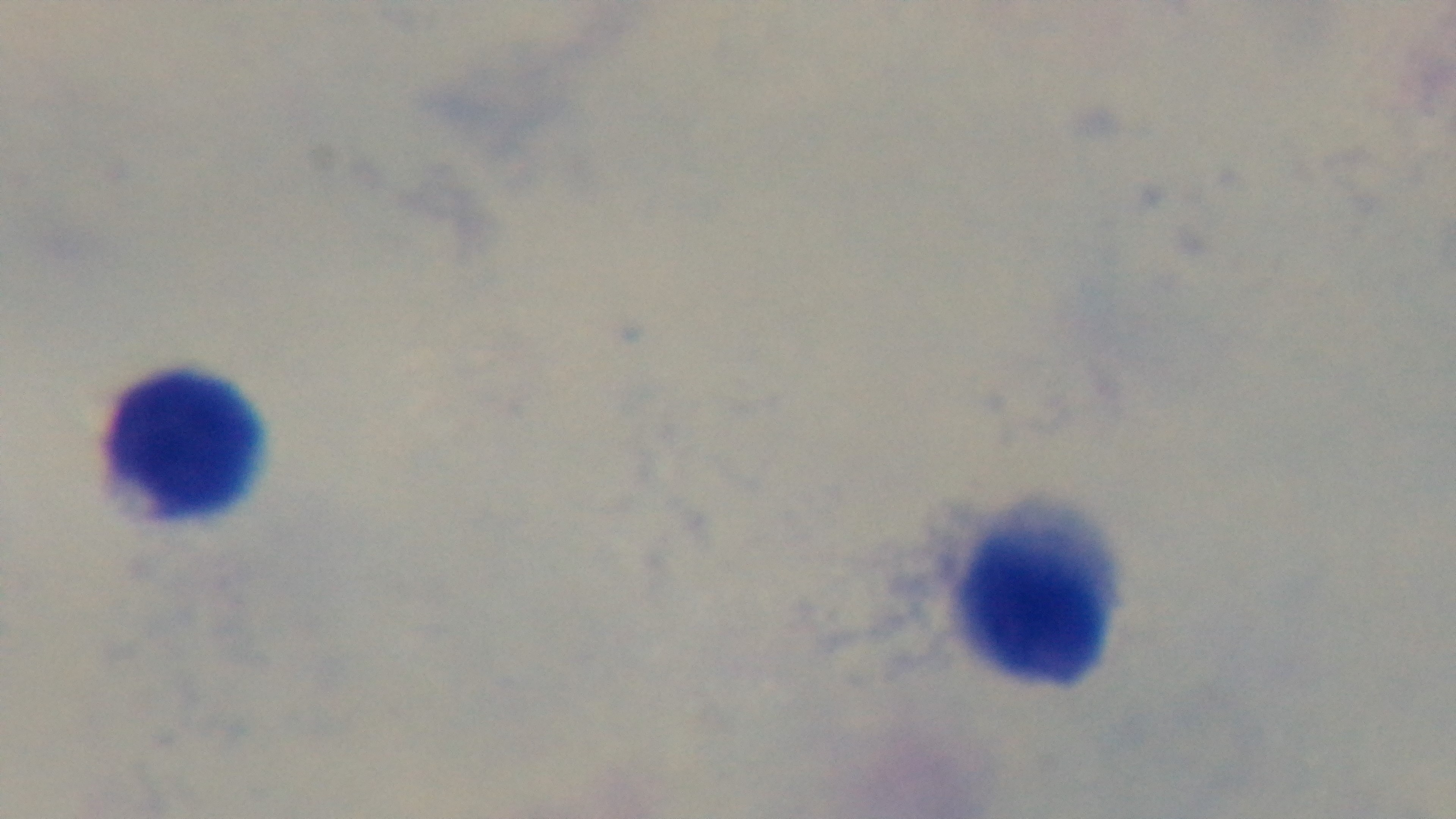
modality = light microscopy
malaria status = uninfected
capture = mounted 4K digital camera
objective = 100x oil immersion
stain = Giemsa
preparation = thick blood film
field of view = single